Locate every Plasmodium malariae-infected red blood cell.
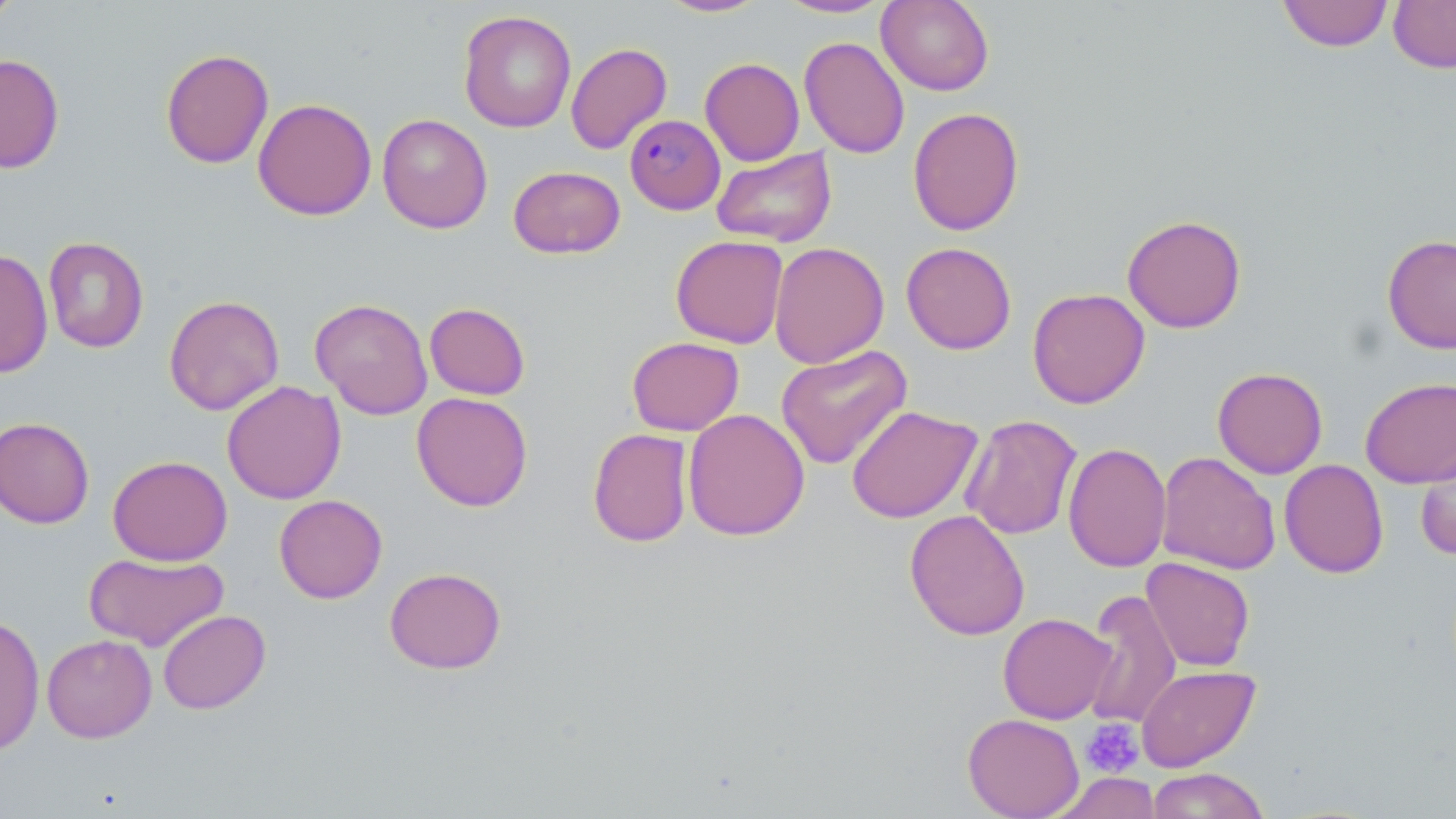
Approximate bounding boxes as (x1,y1)-(x2,y2) corner pairs in pixels.
Plasmodium malariae-infected red blood cells: (624,114)-(726,214).

Summary:
  - Uninfected red blood cell locations: (0,0)-(22,25), (658,0)-(771,18), (774,0)-(892,19), (876,0)-(994,96), (1277,0)-(1394,52), (1388,0)-(1456,73), (458,10)-(576,133), (799,37)-(910,158), (566,43)-(672,155), (160,48)-(274,169), (0,53)-(64,173), (700,58)-(805,166), (253,98)-(377,221), (908,107)-(1025,236), (377,114)-(492,234), (711,147)-(837,247), (508,165)-(626,259), (1121,214)-(1247,333), (1382,233)-(1456,354), (670,235)-(789,348), (43,236)-(149,353), (769,241)-(889,369), (901,242)-(1016,354), (0,248)-(53,378), (1027,287)-(1150,408), (163,295)-(285,415), (310,298)-(433,419), (424,302)-(530,400), (627,336)-(744,436), (775,344)-(913,470), (1212,367)-(1328,479), (1359,376)-(1456,488), (222,381)-(346,505), (411,392)-(533,512), (846,404)-(982,524), (682,409)-(810,541), (960,414)-(1083,540), (0,416)-(95,529), (587,428)-(694,547), (1415,440)-(1456,560), (1063,441)-(1171,572), (1156,451)-(1281,575), (107,455)-(232,566), (1279,459)-(1389,578), (274,494)-(387,604), (904,509)-(1030,641), (85,553)-(228,651), (1141,557)-(1255,671), (384,567)-(506,674), (1081,589)-(1182,730), (157,609)-(271,714), (997,613)-(1117,724), (0,614)-(45,754), (42,634)-(157,743), (1136,665)-(1260,772), (962,713)-(1084,819), (1146,767)-(1270,818), (1047,772)-(1163,819)
  - Platelet locations: (1080,719)-(1144,778)
  - Slide-level diagnosis: Plasmodium malariae
  - Modality: light microscopy
  - Preparation: thin blood smear
  - Magnification: 1000x
  - Field of view: one of a larger specimen
  - Stain: May-Grünwald-Giemsa
  - Image size: 1456×819 pixels